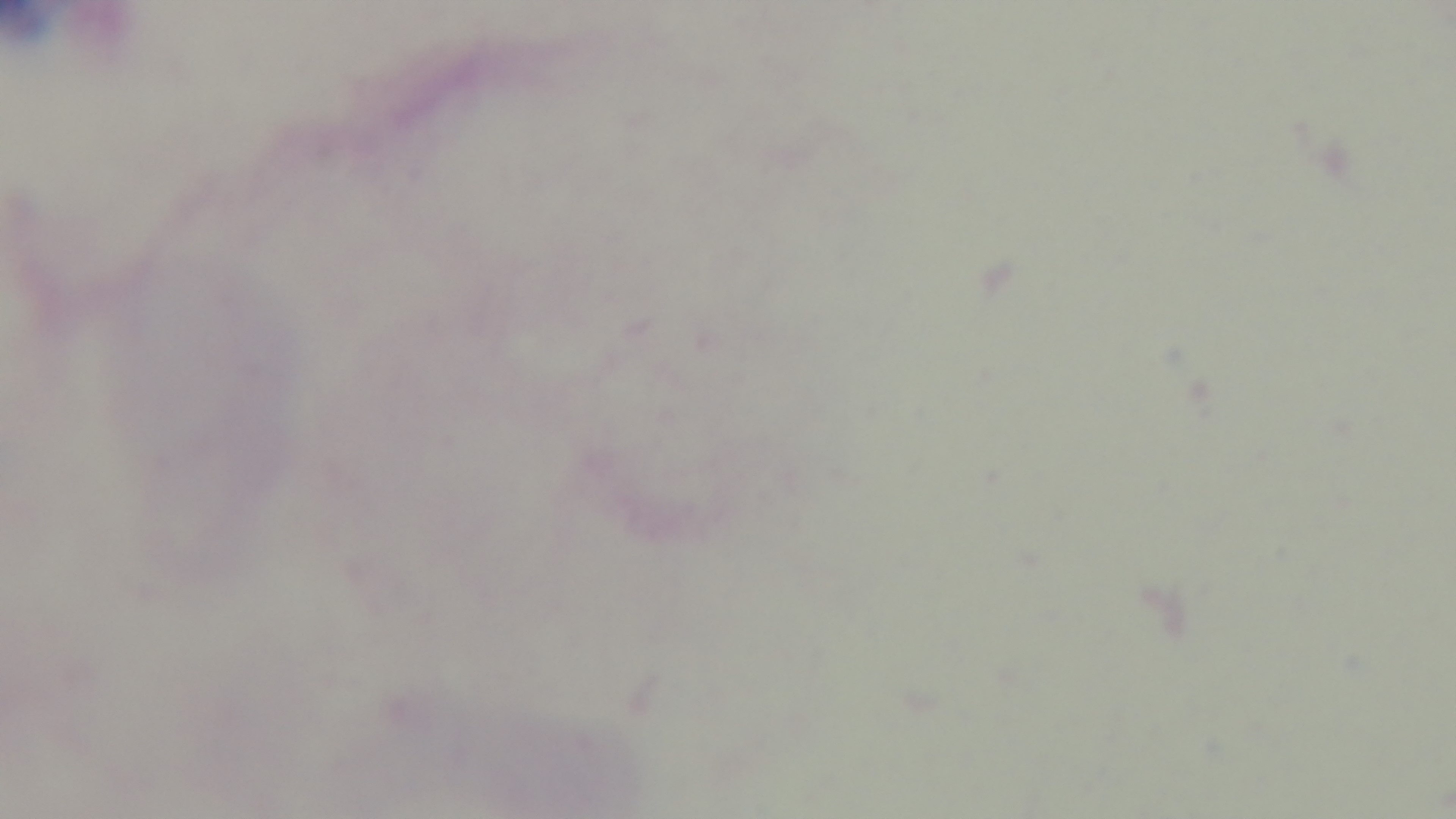

Summary:
  - Malaria status: uninfected
  - Modality: light microscopy
  - Stain: Giemsa
  - Preparation: thick smear
  - Field of view: one from the slide
  - Objective: 100x oil immersion
  - Capture: mounted 4K digital camera